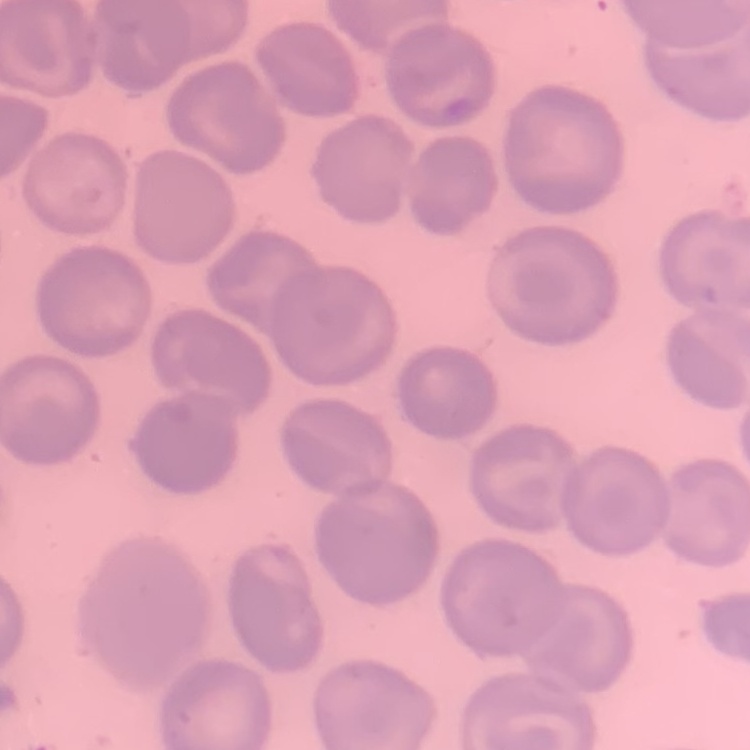
Summary:
  - Red blood cell morphology: no rouleaux formation
  - Preparation: thin blood smear
  - Stain: Field's or Giemsa
  - Image type: one tile cut from a larger photomicrograph